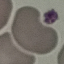 Malaria status: uninfected. Thin smear of blood. Giemsa-stained preparation. Cell patch, automatically extracted from a larger field of view and resized to 64 × 64 pixels. Acquired by smartphone through the microscope eyepiece.